Give the preparation type.
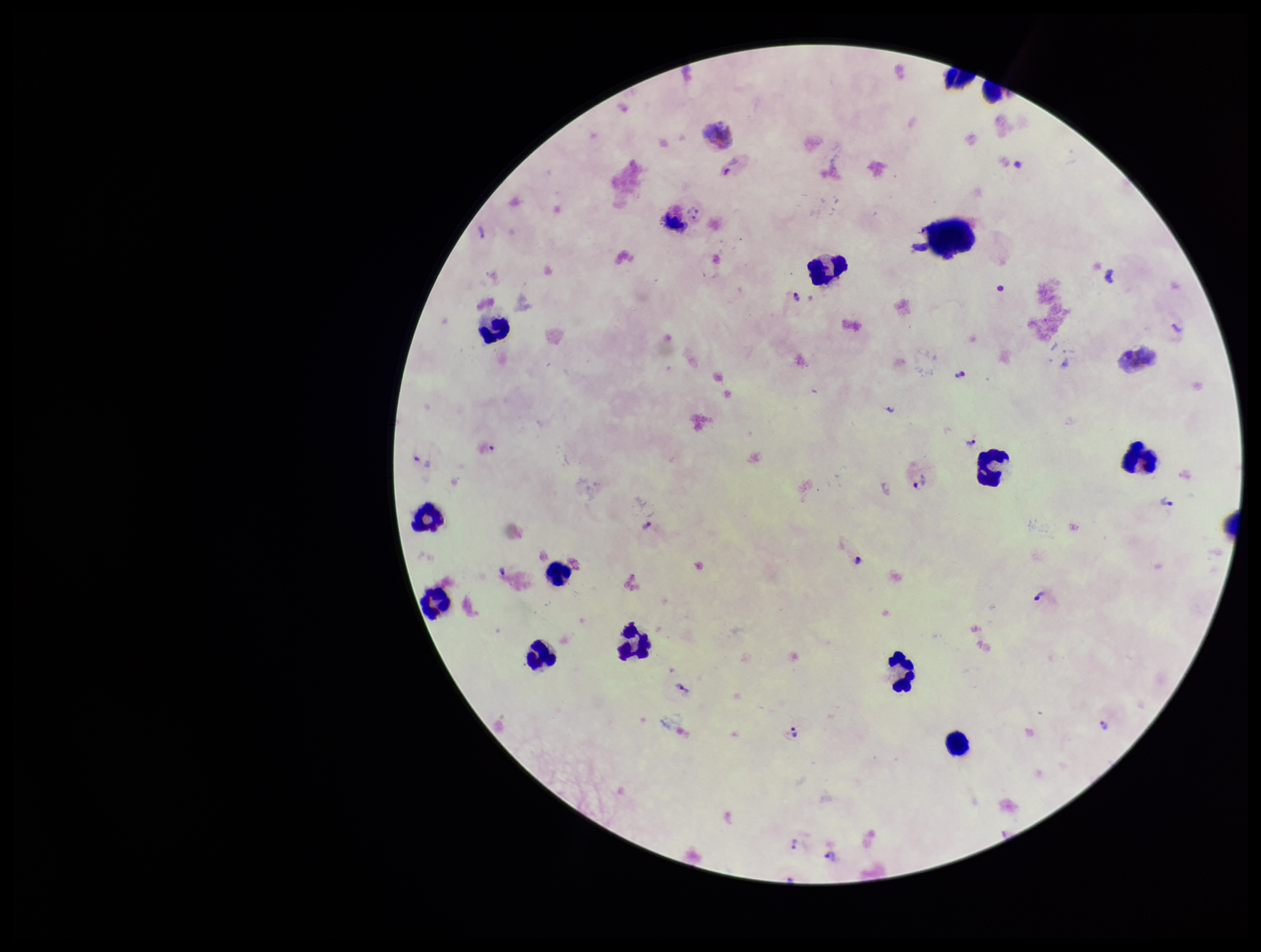
A thick smear.

{
  "leukocyte_count": 15,
  "plasmodium_parasites": "identified",
  "species_reported_for_this_patient": "Plasmodium vivax",
  "parasite_count": 16,
  "patient_malaria_status": "infected",
  "capture": "smartphone photograph through the microscope eyepiece",
  "stain": "Giemsa",
  "image_size": "1261×952 pixels",
  "field_of_view": "one from this slide"
}